Identify the parasite.
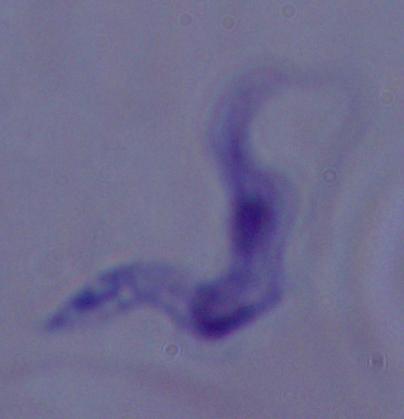
A trypanosome.

Summary:
  - Magnification: 1000x
  - Modality: photomicrograph